Classify this cell by malaria status.
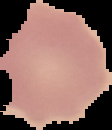
It is uninfected.

Summary:
  - Preparation: thin blood film
  - Image size: 112×130 pixels
  - Image type: segmented cell region with the area outside set to black